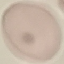
Malaria status: uninfected. Automatically extracted cell patch, resized to 64 × 64 pixels. Giemsa-stained preparation. Thin blood film. Acquired by smartphone through the microscope eyepiece.